Identify the cell.
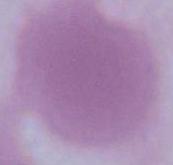
An erythrocyte.

Micrograph. Captured at 1000x magnification.